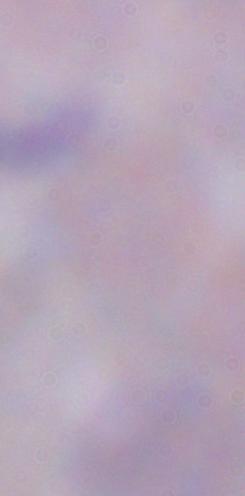

identification = trypanosome
modality = micrograph
magnification = 1000x